Classify this cell by malaria status.
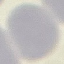
Uninfected.

Thin blood film. Automatically extracted cell patch, resized to 64 × 64 pixels. Photographed with a smartphone camera at the microscope eyepiece. Giemsa stain.